State the preparation type.
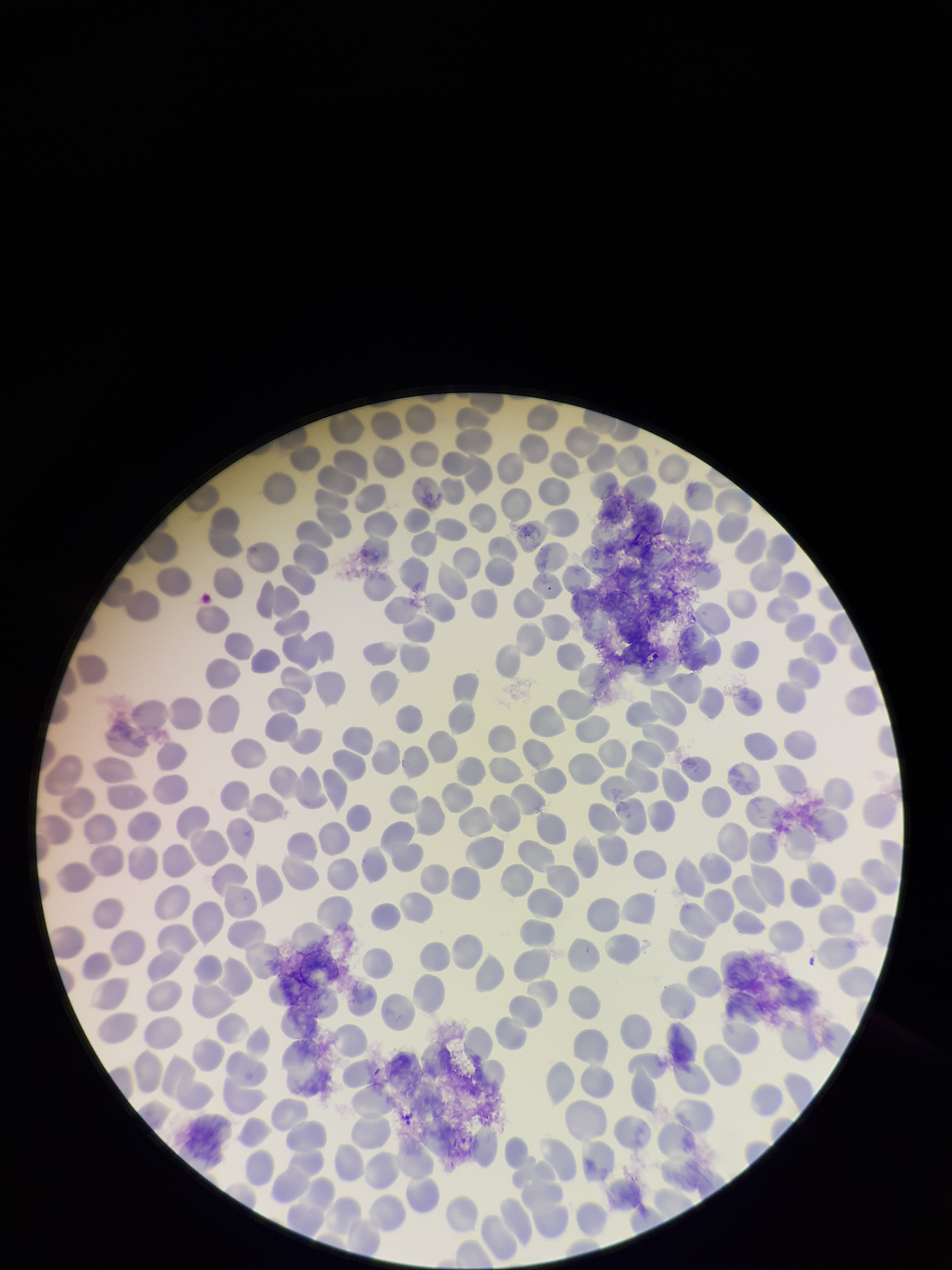
A thin smear.

Patient malaria status: negative. Red blood cell count: 315. Parasitized red blood cell count: 0. Single field of view. Parasitized red blood cells: none seen. Stained with Giemsa. Image is 952×1270 pixels. Photographed through the microscope eyepiece with a smartphone camera.